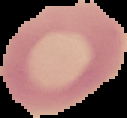

Summary:
  - Malaria status: uninfected
  - Image size: 127×118 pixels
  - Preparation: thin blood film
  - Image type: segmented cell region on a black background